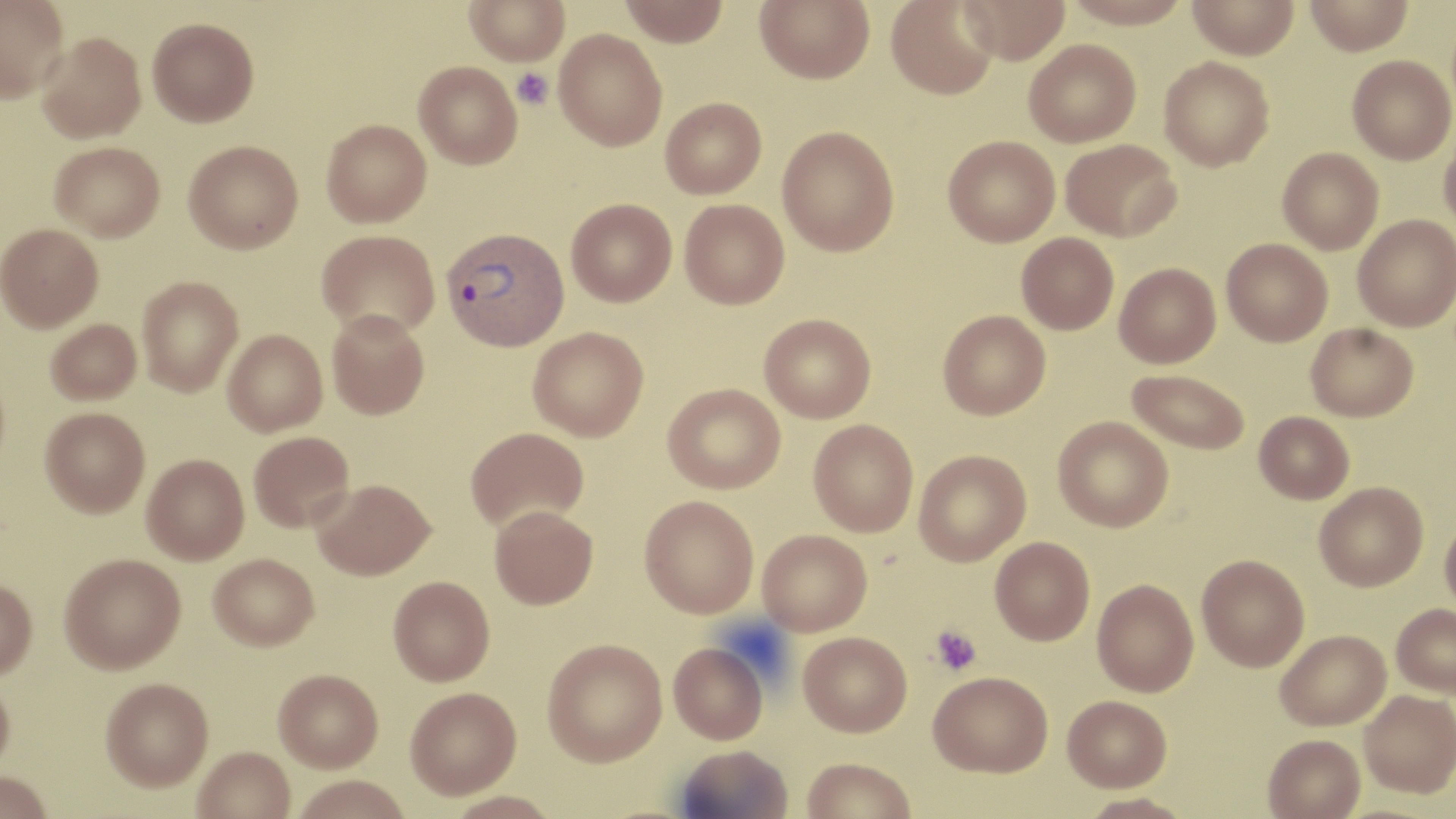
Approximate bounding boxes as named x1/y1/x2/y2 corners in pixels. Platelet locations: (x1=512, y1=68, x2=554, y2=110), (x1=929, y1=625, x2=982, y2=677). Plasmodium vivax-infected red blood cell locations: (x1=441, y1=226, x2=569, y2=351). Uninfected red blood cell locations: (x1=0, y1=0, x2=70, y2=102), (x1=465, y1=0, x2=569, y2=66), (x1=619, y1=0, x2=729, y2=46), (x1=754, y1=0, x2=875, y2=83), (x1=886, y1=0, x2=1000, y2=100), (x1=959, y1=0, x2=1070, y2=64), (x1=1061, y1=0, x2=1193, y2=29), (x1=1186, y1=0, x2=1300, y2=59), (x1=1305, y1=0, x2=1413, y2=55), (x1=147, y1=17, x2=259, y2=126), (x1=554, y1=29, x2=668, y2=151), (x1=37, y1=32, x2=146, y2=143), (x1=1024, y1=39, x2=1141, y2=147), (x1=1347, y1=55, x2=1455, y2=164), (x1=1159, y1=56, x2=1274, y2=171), (x1=414, y1=61, x2=522, y2=169), (x1=661, y1=97, x2=767, y2=198), (x1=322, y1=119, x2=432, y2=227), (x1=777, y1=125, x2=900, y2=256), (x1=1439, y1=131, x2=1456, y2=235), (x1=943, y1=135, x2=1060, y2=247), (x1=1061, y1=139, x2=1182, y2=242), (x1=184, y1=140, x2=303, y2=253), (x1=49, y1=141, x2=164, y2=241), (x1=1277, y1=147, x2=1384, y2=254), (x1=566, y1=198, x2=676, y2=306), (x1=679, y1=199, x2=789, y2=309), (x1=1353, y1=215, x2=1456, y2=332), (x1=0, y1=223, x2=103, y2=331), (x1=317, y1=229, x2=440, y2=338), (x1=1016, y1=232, x2=1119, y2=335), (x1=1221, y1=238, x2=1333, y2=346), (x1=1114, y1=263, x2=1221, y2=368), (x1=137, y1=275, x2=244, y2=396), (x1=937, y1=309, x2=1051, y2=420), (x1=327, y1=310, x2=429, y2=419), (x1=759, y1=313, x2=876, y2=423), (x1=46, y1=318, x2=142, y2=405), (x1=1306, y1=322, x2=1418, y2=421), (x1=528, y1=326, x2=649, y2=441), (x1=223, y1=329, x2=328, y2=435), (x1=1127, y1=368, x2=1250, y2=454), (x1=663, y1=383, x2=785, y2=493), (x1=40, y1=407, x2=150, y2=517), (x1=1254, y1=411, x2=1354, y2=504), (x1=1053, y1=416, x2=1173, y2=532), (x1=809, y1=419, x2=919, y2=536), (x1=465, y1=427, x2=589, y2=532), (x1=249, y1=431, x2=354, y2=532), (x1=914, y1=450, x2=1031, y2=566), (x1=142, y1=453, x2=249, y2=564), (x1=313, y1=479, x2=434, y2=579), (x1=1314, y1=482, x2=1428, y2=591), (x1=639, y1=495, x2=759, y2=618), (x1=489, y1=505, x2=598, y2=610), (x1=1440, y1=515, x2=1456, y2=618), (x1=757, y1=529, x2=872, y2=635), (x1=990, y1=537, x2=1095, y2=646), (x1=59, y1=553, x2=185, y2=673), (x1=209, y1=553, x2=319, y2=650), (x1=1197, y1=554, x2=1309, y2=671), (x1=388, y1=576, x2=495, y2=686), (x1=0, y1=578, x2=37, y2=680), (x1=1092, y1=578, x2=1198, y2=696), (x1=1391, y1=603, x2=1456, y2=697), (x1=1276, y1=629, x2=1391, y2=730), (x1=798, y1=632, x2=912, y2=736), (x1=542, y1=638, x2=667, y2=767), (x1=669, y1=642, x2=768, y2=743), (x1=273, y1=668, x2=383, y2=772), (x1=929, y1=671, x2=1053, y2=777), (x1=0, y1=675, x2=15, y2=779), (x1=100, y1=677, x2=213, y2=791), (x1=405, y1=687, x2=521, y2=799), (x1=1359, y1=690, x2=1456, y2=797), (x1=1063, y1=695, x2=1171, y2=792), (x1=1263, y1=733, x2=1365, y2=819), (x1=675, y1=744, x2=793, y2=819), (x1=193, y1=747, x2=295, y2=819), (x1=800, y1=757, x2=917, y2=819), (x1=0, y1=771, x2=54, y2=819), (x1=291, y1=775, x2=413, y2=819), (x1=1076, y1=793, x2=1196, y2=818). Slide-level diagnosis: Plasmodium vivax. Image is 1456×819 pixels. May-Grünwald-Giemsa stain. Single field of view. Thin blood smear. Optical microscopy. Captured at 1000x magnification.